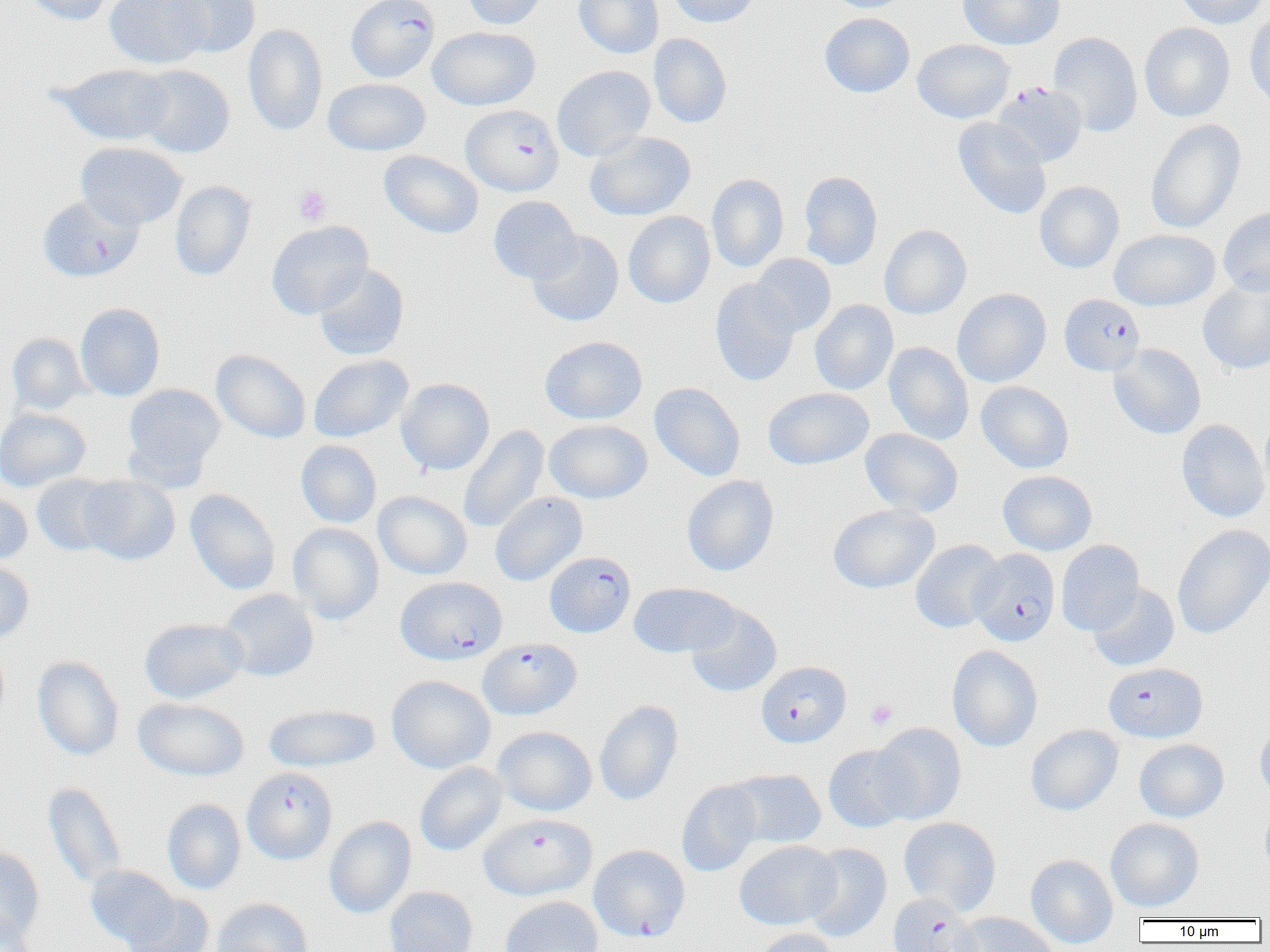
Summary:
  - Coordinate format: approximate bounding boxes as [x1, y1, x2, y2] in pixels
  - Uninfected red blood cell locations: [21, 0, 121, 26], [105, 0, 211, 69], [161, 0, 260, 57], [463, 0, 547, 30], [574, 0, 664, 59], [668, 0, 760, 27], [823, 0, 914, 13], [957, 0, 1064, 50], [1175, 0, 1267, 29], [1245, 10, 1270, 112], [820, 13, 915, 97], [1139, 22, 1235, 122], [243, 24, 328, 136], [427, 26, 540, 110], [1049, 32, 1142, 137], [649, 33, 732, 128], [912, 39, 1015, 123], [54, 64, 175, 146], [136, 65, 234, 158], [552, 65, 655, 161], [323, 78, 431, 156], [953, 118, 1052, 219], [1145, 119, 1246, 234], [584, 131, 696, 221], [75, 142, 187, 229], [379, 150, 483, 239], [798, 171, 883, 270], [707, 174, 789, 273], [170, 181, 255, 280], [1035, 181, 1124, 273], [488, 196, 582, 284], [1218, 206, 1270, 296], [623, 211, 715, 308], [266, 220, 373, 319], [879, 225, 972, 319], [1109, 229, 1220, 310], [528, 231, 624, 326], [751, 253, 836, 336], [313, 264, 409, 360], [1198, 278, 1270, 375], [710, 279, 801, 385], [952, 288, 1051, 387], [810, 300, 898, 395], [75, 303, 165, 401], [7, 333, 89, 415], [540, 336, 647, 424], [884, 342, 973, 445], [1109, 343, 1206, 440], [211, 349, 311, 444], [308, 355, 413, 443], [396, 378, 495, 475], [975, 381, 1074, 473], [649, 382, 745, 481], [123, 384, 224, 478], [763, 387, 874, 469], [0, 407, 90, 492], [1259, 413, 1270, 510], [1177, 419, 1269, 522], [544, 420, 652, 503], [458, 426, 549, 534], [860, 428, 963, 518], [296, 440, 382, 528], [998, 470, 1097, 555], [32, 474, 121, 556], [681, 475, 779, 577], [77, 476, 180, 565], [184, 489, 280, 594], [0, 491, 33, 564], [373, 491, 472, 580], [490, 492, 587, 586], [828, 504, 940, 593], [288, 523, 384, 624], [1172, 524, 1270, 639], [910, 540, 1005, 633], [1055, 540, 1144, 636], [0, 559, 34, 645], [629, 583, 738, 658], [1087, 583, 1179, 672], [218, 589, 318, 682], [685, 604, 783, 697], [139, 618, 249, 703], [0, 638, 10, 725], [947, 646, 1042, 752], [32, 656, 123, 760], [387, 676, 495, 774], [133, 697, 248, 780], [594, 700, 683, 806], [263, 704, 380, 772], [1255, 721, 1270, 806], [871, 723, 967, 824], [1026, 724, 1123, 816], [492, 726, 597, 816], [1134, 739, 1228, 822], [824, 744, 916, 832], [414, 763, 508, 856], [729, 769, 826, 849], [676, 780, 763, 877], [43, 782, 127, 889], [162, 799, 246, 894], [1260, 803, 1270, 882], [324, 816, 416, 918], [899, 817, 1001, 916], [1105, 818, 1204, 912], [734, 840, 840, 930], [803, 844, 892, 942], [0, 846, 45, 943], [1026, 854, 1118, 949], [86, 865, 179, 948], [384, 886, 478, 952], [122, 893, 215, 952], [500, 896, 603, 952], [212, 898, 313, 952], [0, 911, 38, 952], [954, 911, 1058, 952], [751, 928, 840, 952]
  - Platelet locations: [294, 185, 331, 225], [866, 700, 897, 729]
  - Plasmodium falciparum-infected red blood cell locations: [346, 0, 440, 83], [992, 82, 1087, 166], [461, 105, 564, 196], [37, 194, 143, 282], [1060, 294, 1144, 375], [970, 549, 1061, 647], [544, 551, 635, 637], [396, 576, 507, 665], [478, 638, 581, 719], [756, 661, 850, 748], [1104, 662, 1207, 743], [242, 767, 337, 864], [479, 814, 595, 900], [589, 844, 690, 942], [887, 893, 982, 952]
  - Slide-level diagnosis: Plasmodium falciparum
  - Magnification: 1000x
  - Image size: 1270×952 pixels
  - Field of view: single
  - Modality: light microscopy
  - Preparation: thin blood film